State which cell type is depicted.
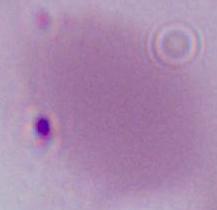
This is an erythrocyte.

{
  "modality": "photomicrograph",
  "magnification": "1000x"
}